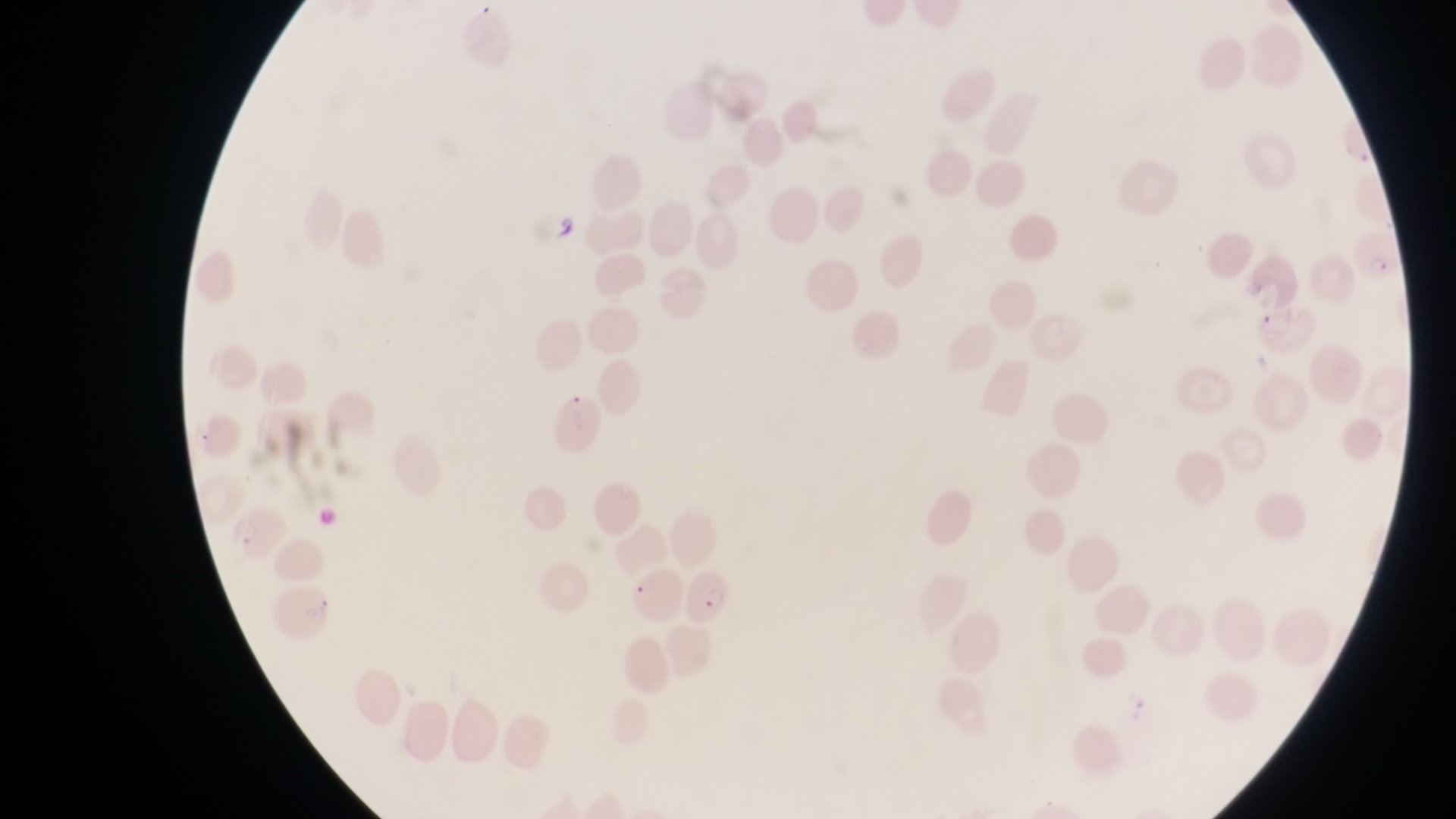 Approximate bounding boxes as {left, top, right, bottom} in pixels. Parasitised red blood cell locations: {1351, 230, 1401, 286}, {547, 383, 602, 452}, {631, 561, 680, 620}, {684, 568, 737, 628}. Image is 1456×819 pixels. Photographed through the eyepiece of an Olympus CX-23 microscope with a smartphone camera. Magnification of 1000x. One field of view. Thin blood film. Collected in Uganda.